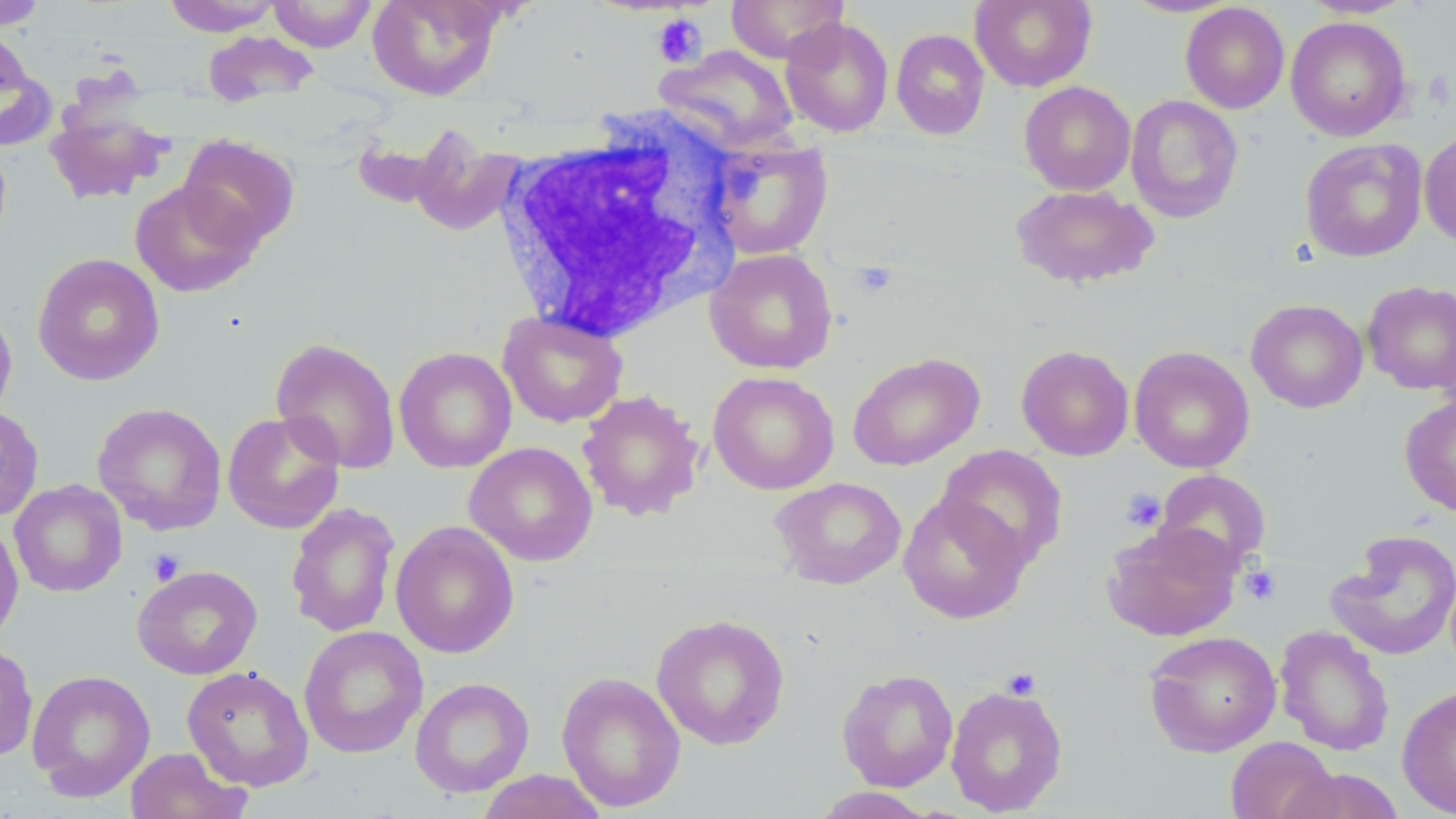

Summary:
  - Coordinate format: approximate bounding boxes as [x1, y1, x2, y2] in pixels
  - Platelet locations: [652, 14, 707, 67], [851, 261, 898, 300], [1121, 488, 1166, 532], [147, 549, 186, 585], [1240, 564, 1282, 605], [1001, 667, 1041, 701]
  - Uninfected red blood cell locations: [0, 0, 46, 30], [267, 0, 376, 52], [367, 0, 504, 101], [726, 0, 849, 63], [970, 0, 1096, 91], [1120, 0, 1241, 17], [1299, 0, 1415, 18], [162, 1, 282, 35], [1180, 3, 1290, 113], [1286, 16, 1411, 141], [780, 17, 894, 136], [890, 28, 990, 139], [0, 30, 55, 151], [202, 30, 320, 109], [655, 44, 799, 153], [1019, 81, 1136, 195], [1126, 95, 1244, 223], [45, 105, 171, 204], [407, 125, 524, 238], [1419, 130, 1456, 248], [178, 134, 300, 251], [707, 137, 833, 260], [1300, 138, 1428, 262], [129, 181, 262, 298], [1009, 183, 1159, 290], [704, 248, 838, 374], [32, 253, 165, 387], [1362, 280, 1456, 396], [1246, 299, 1368, 414], [0, 300, 17, 425], [497, 310, 628, 428], [271, 337, 401, 474], [1016, 344, 1134, 461], [394, 346, 517, 473], [1129, 346, 1255, 473], [847, 351, 984, 471], [708, 371, 839, 494], [577, 389, 705, 522], [1400, 394, 1456, 517], [92, 402, 228, 535], [0, 405, 44, 522], [222, 410, 346, 534], [464, 441, 598, 566], [935, 444, 1068, 570], [1154, 469, 1272, 574], [770, 477, 907, 590], [9, 480, 127, 598], [898, 493, 1031, 623], [285, 502, 400, 638], [0, 518, 23, 647], [390, 521, 519, 659], [1102, 521, 1242, 642], [1327, 529, 1456, 661], [132, 565, 262, 679], [651, 613, 790, 750], [298, 625, 428, 759], [1275, 626, 1394, 756], [1143, 629, 1282, 757], [0, 641, 38, 763], [181, 666, 314, 791], [837, 668, 959, 791], [27, 669, 156, 802], [556, 670, 686, 812], [410, 677, 534, 798], [945, 683, 1068, 816], [1397, 685, 1456, 817], [1225, 737, 1340, 819], [124, 747, 250, 819], [1278, 767, 1405, 819], [475, 769, 609, 819], [810, 787, 936, 818]
  - White blood cell locations: [498, 112, 744, 344]
  - Slide-level diagnosis: negative for blood parasites
  - Modality: light microscopy
  - Stain: May-Grünwald-Giemsa
  - Preparation: thin blood smear
  - Image size: 1456×819 pixels
  - Magnification: 1000x
  - Field of view: one of a larger specimen